Classify this cell by malaria status.
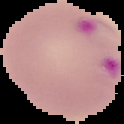

It is parasitized.

Image is 124×124 pixels. The area outside the segmented cell region is set to black. From a thin blood film.